Classify this cell by malaria status.
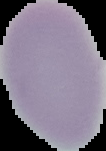

Uninfected.

image size = 106×151 pixels
image type = segmented cell region with the area outside set to black
preparation = thin blood smear